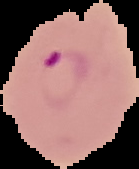

image size = 139×169 pixels
preparation = thin blood film
malaria status = parasitized
image type = segmented cell region with the area outside set to black